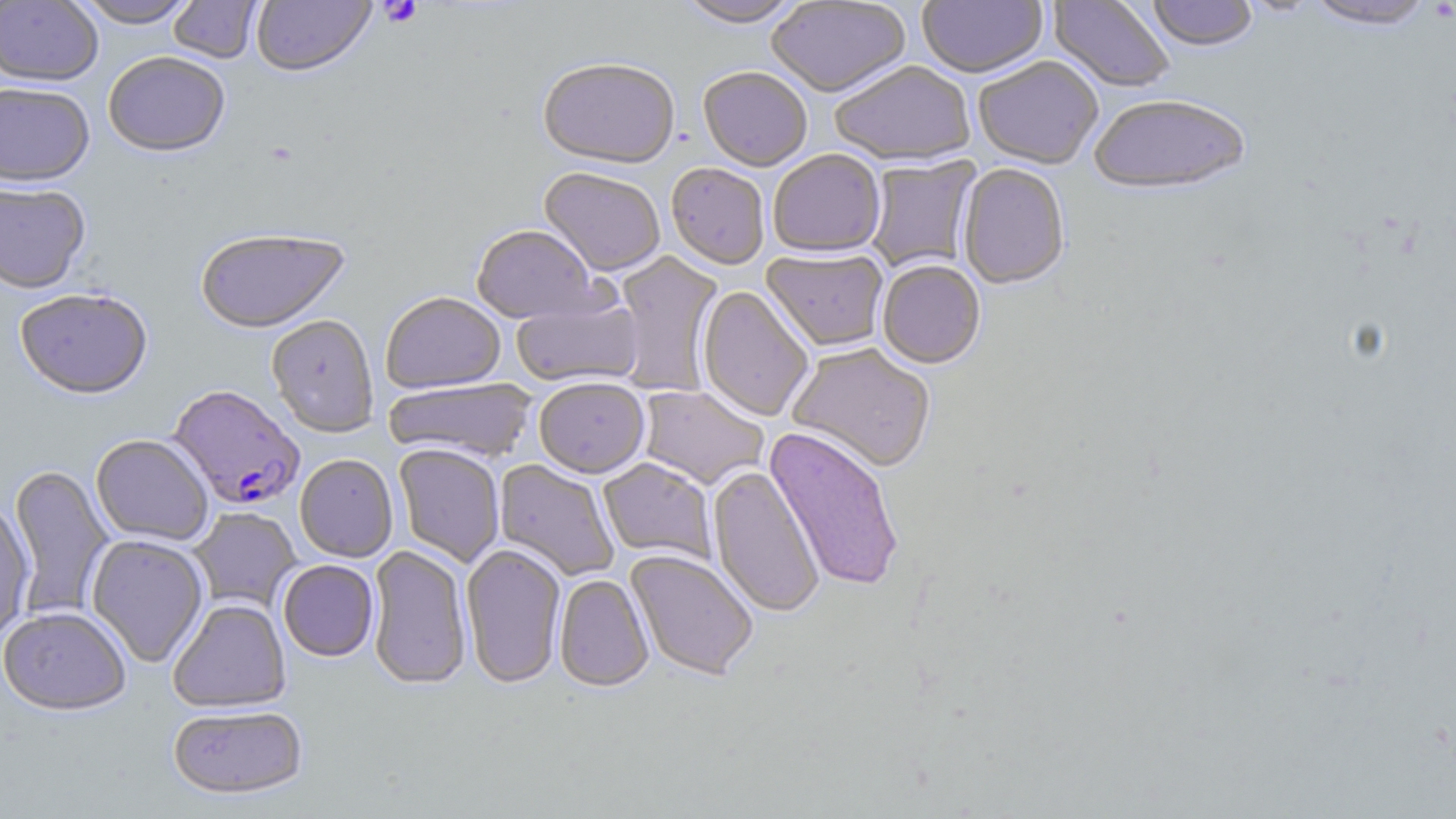
Summary:
  - Coordinate format: approximate bounding boxes as (x1, y1, x2, y2) in pixels
  - Platelet locations: (379, 1, 423, 28)
  - Plasmodium falciparum-infected red blood cell locations: (168, 386, 305, 510)
  - Uninfected red blood cell locations: (0, 0, 103, 89), (73, 0, 198, 30), (168, 0, 263, 65), (676, 0, 804, 30), (766, 0, 913, 100), (918, 0, 1048, 81), (1047, 0, 1175, 95), (1147, 0, 1258, 54), (1237, 0, 1324, 17), (1303, 0, 1437, 32), (251, 1, 376, 80), (104, 54, 229, 160), (974, 57, 1103, 171), (537, 61, 680, 172), (831, 63, 976, 169), (698, 69, 812, 173), (0, 85, 95, 192), (1089, 97, 1251, 199), (768, 150, 886, 260), (865, 156, 981, 274), (666, 165, 769, 272), (957, 165, 1070, 291), (538, 169, 664, 279), (0, 185, 91, 296), (471, 226, 603, 326), (194, 230, 351, 336), (761, 250, 889, 354), (612, 251, 725, 396), (877, 261, 986, 371), (697, 286, 814, 423), (15, 291, 153, 402), (381, 293, 505, 394), (511, 295, 643, 389), (266, 315, 379, 439), (787, 344, 936, 475), (384, 378, 536, 465), (535, 380, 650, 480), (638, 385, 769, 490), (764, 428, 904, 593), (90, 435, 213, 546), (393, 444, 504, 568), (295, 455, 398, 563), (598, 458, 716, 564), (494, 459, 619, 581), (8, 464, 115, 618), (707, 466, 825, 619), (0, 503, 35, 642), (190, 508, 302, 613), (86, 535, 209, 668), (461, 544, 566, 689), (366, 545, 472, 691), (625, 550, 758, 682), (278, 560, 379, 663), (554, 576, 654, 693), (168, 600, 291, 713), (1, 608, 132, 717), (167, 705, 308, 802)
  - Slide-level diagnosis: Plasmodium falciparum
  - Magnification: 1000x
  - Preparation: thin blood film
  - Stain: May-Grünwald-Giemsa
  - Field of view: one of a larger specimen
  - Modality: optical microscopy
  - Image size: 1456×819 pixels